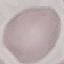

Result: negative for malaria parasites. Giemsa stain. Photographed with a smartphone camera at the microscope eyepiece. Thin blood film. Cell patch, automatically extracted from a larger field of view and resized to 64 × 64 pixels.